Classify this cell by malaria status.
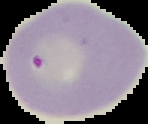
Uninfected.

Summary:
  - Image type: segmented cell region on a black background
  - Preparation: thin blood smear
  - Image size: 148×124 pixels